Assess for parasitized red blood cells.
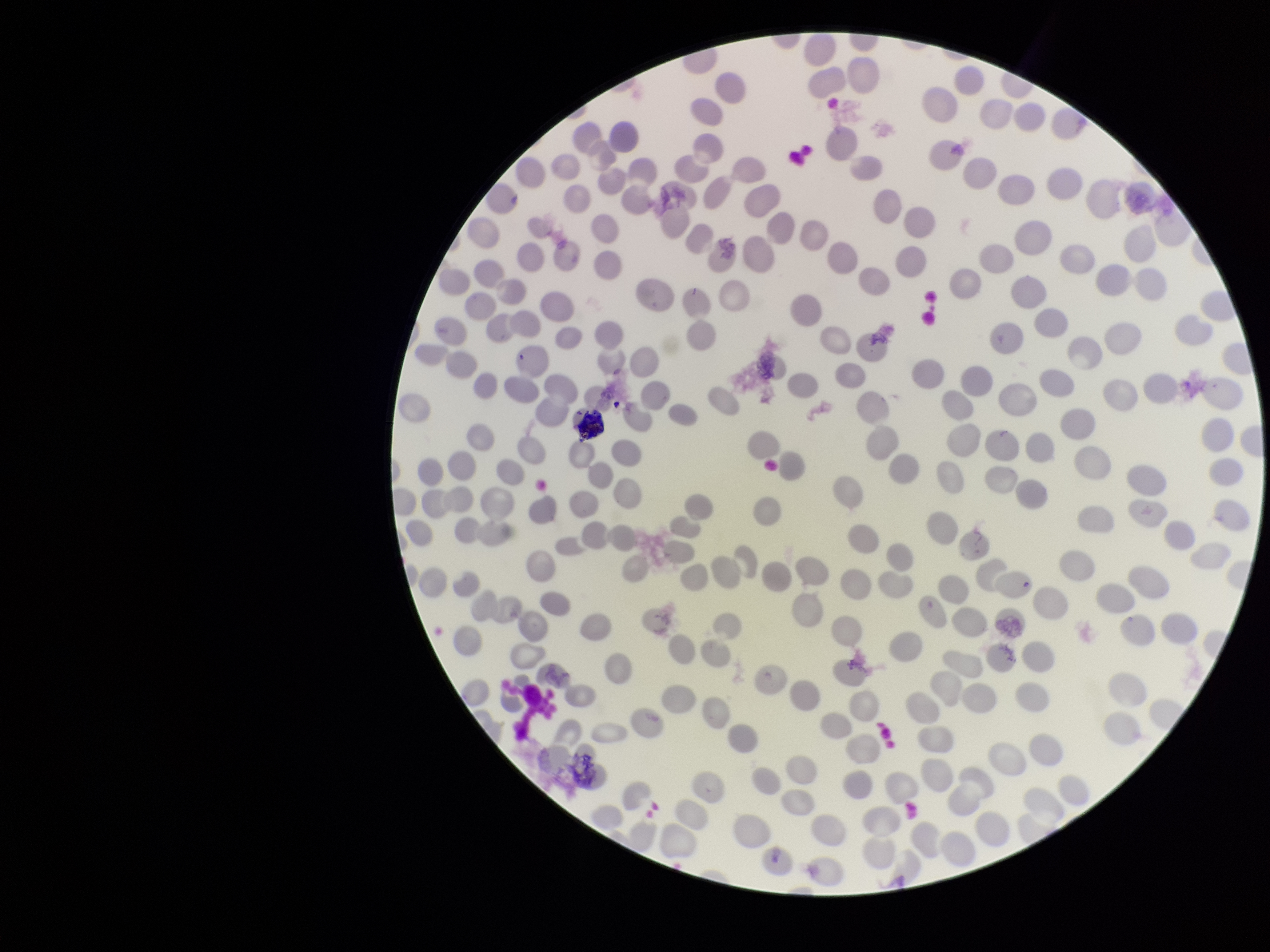
None identified.

Summary:
  - Parasitized red blood cell count: 0
  - Patient malaria status: negative
  - Field of view: one from this slide
  - Capture: smartphone photograph through the microscope eyepiece
  - Red blood cell count: 225
  - Image size: 1270×952 pixels
  - Stain: Giemsa
  - Preparation: thin blood smear